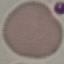
Summary:
  - Result: no malaria parasites seen
  - Stain: Giemsa
  - Preparation: thin smear
  - Capture: smartphone camera at the microscope eyepiece
  - Image type: automatically extracted cell patch, resized to 64 × 64 pixels